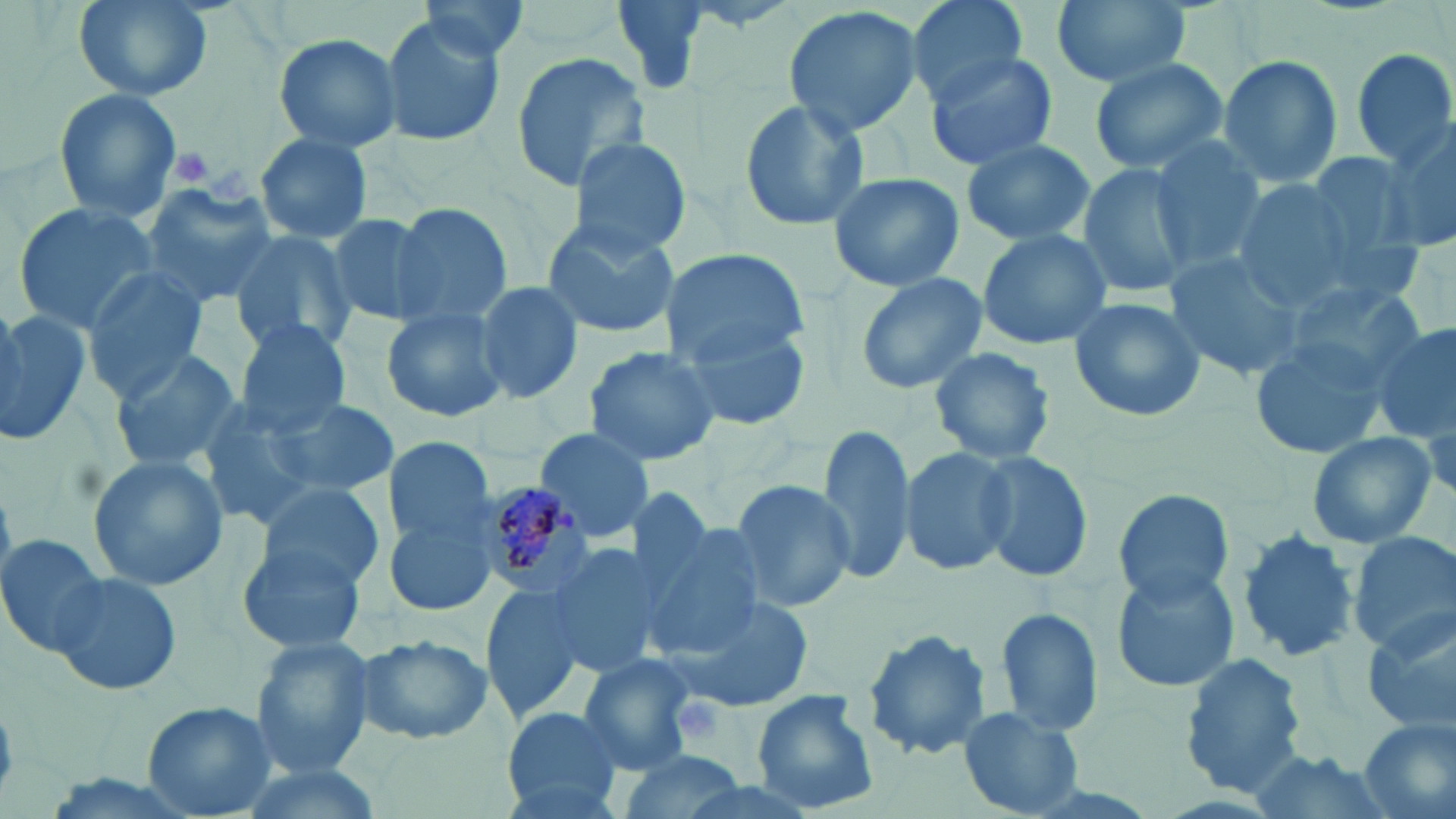 Approximate bounding boxes as (x1, y1, x2, y2) in pixels. Platelet locations: (164, 147, 216, 189), (669, 697, 725, 747). Uninfected red blood cell locations: (73, 0, 214, 104), (416, 0, 530, 68), (908, 0, 1032, 99), (1050, 0, 1192, 90), (608, 1, 714, 95), (781, 5, 926, 140), (379, 14, 507, 147), (271, 31, 404, 154), (1351, 47, 1456, 171), (509, 50, 649, 193), (923, 51, 1059, 171), (1216, 55, 1345, 189), (1086, 57, 1231, 175), (53, 87, 183, 220), (736, 97, 873, 231), (1365, 132, 1456, 253), (256, 133, 373, 243), (567, 135, 693, 257), (958, 138, 1096, 246), (1150, 138, 1267, 274), (1301, 148, 1437, 262), (1075, 161, 1196, 300), (828, 171, 965, 291), (1227, 179, 1369, 313), (142, 186, 277, 308), (10, 201, 161, 334), (393, 204, 512, 323), (324, 213, 440, 326), (542, 218, 678, 341), (975, 228, 1113, 350), (228, 229, 358, 357), (662, 249, 811, 370), (1163, 251, 1302, 379), (80, 266, 211, 398), (853, 272, 989, 394), (474, 282, 584, 404), (1285, 282, 1429, 392), (1066, 296, 1207, 424), (379, 305, 509, 424), (0, 309, 88, 441), (670, 317, 812, 434), (233, 320, 353, 434), (1367, 320, 1456, 443), (1250, 335, 1390, 458), (583, 345, 723, 468), (928, 346, 1057, 464), (110, 347, 242, 473), (198, 394, 321, 532), (268, 398, 396, 498), (818, 422, 914, 584), (533, 427, 657, 539), (1305, 431, 1437, 550), (384, 435, 498, 552), (899, 446, 1019, 578), (978, 452, 1095, 583), (85, 455, 227, 592), (727, 479, 856, 612), (259, 481, 386, 591), (1111, 487, 1235, 607), (384, 489, 500, 617), (637, 517, 770, 658), (1238, 531, 1359, 661), (1348, 531, 1455, 652), (0, 535, 113, 656), (234, 541, 365, 655), (543, 543, 667, 673), (1109, 565, 1240, 694), (49, 570, 182, 696), (480, 581, 593, 726), (671, 593, 814, 710), (996, 607, 1104, 735), (1362, 613, 1456, 734), (860, 627, 992, 760), (353, 634, 496, 746), (248, 638, 377, 780), (576, 653, 696, 774), (1180, 653, 1311, 799), (751, 691, 878, 815), (142, 701, 275, 818), (498, 705, 627, 819), (957, 708, 1084, 818), (1356, 715, 1455, 819), (618, 748, 749, 819), (1249, 751, 1392, 819), (222, 762, 391, 819), (665, 775, 823, 819). Plasmodium malariae-infected red blood cell locations: (476, 481, 596, 598). Slide-level diagnosis: Plasmodium malariae. May-Grünwald-Giemsa stain. 1000x magnification. Thin blood film. Light microscopy. One field of a larger specimen. Image is 1456×819 pixels.